Name the parasite shown.
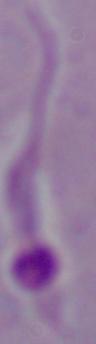
This is Leishmania.

Photomicrograph. Captured at 1000x magnification.